Identify the parasite.
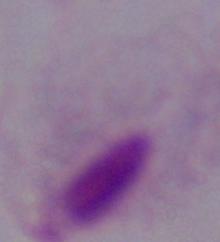
A trichomonad.

modality: micrograph
magnification: 1000x